Locate and identify every blood parasite.
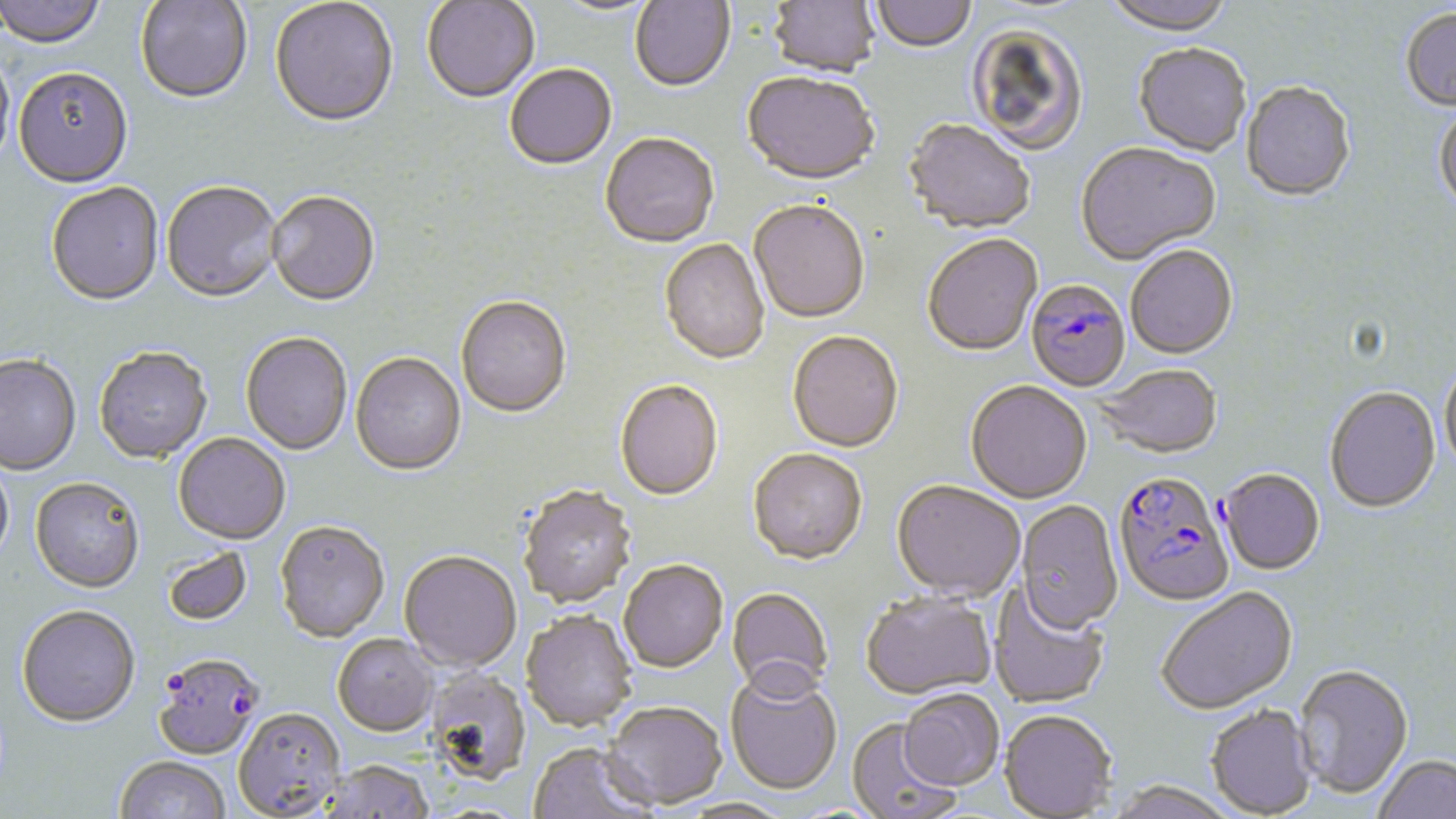

Approximate bounding boxes as (x1, y1, x2, y2) in pixels.
Plasmodium falciparum-infected red blood cells: (1026, 279, 1131, 393), (1218, 469, 1325, 576), (1113, 471, 1235, 609), (152, 653, 264, 762).
No Plasmodium ovale, Plasmodium malariae, Plasmodium vivax, Babesia divergens, or Trypanosoma brucei observed.

Uninfected red blood cell locations: (0, 0, 106, 51), (134, 0, 253, 107), (270, 0, 399, 130), (630, 0, 735, 93), (768, 0, 880, 80), (871, 0, 976, 55), (1102, 0, 1236, 39), (422, 1, 540, 105), (546, 1, 663, 18), (1400, 8, 1456, 114), (967, 24, 1090, 156), (1133, 46, 1251, 158), (0, 49, 14, 179), (505, 66, 617, 172), (13, 70, 133, 190), (741, 74, 879, 188), (1241, 82, 1355, 203), (1434, 104, 1456, 217), (904, 121, 1036, 235), (600, 135, 720, 250), (1076, 144, 1221, 267), (161, 183, 282, 305), (46, 184, 165, 308), (267, 193, 380, 308), (749, 202, 870, 325), (922, 236, 1043, 358), (659, 239, 770, 367), (1126, 246, 1238, 361), (455, 298, 572, 420), (787, 332, 903, 453), (240, 334, 352, 456), (93, 348, 212, 465), (350, 353, 466, 477), (0, 356, 82, 476), (1439, 360, 1456, 477), (1094, 365, 1224, 459), (615, 381, 723, 502), (965, 381, 1092, 504), (1325, 386, 1441, 513), (173, 433, 291, 545), (747, 449, 867, 565), (0, 453, 14, 572), (30, 479, 145, 595), (891, 480, 1025, 601), (518, 487, 638, 610), (1015, 500, 1123, 634), (275, 522, 390, 643), (161, 546, 253, 627), (399, 552, 521, 673), (619, 561, 727, 673), (989, 584, 1110, 709), (1157, 586, 1298, 716), (727, 587, 834, 699), (860, 592, 997, 701), (15, 606, 141, 728), (520, 611, 638, 733), (332, 635, 439, 738), (1294, 664, 1413, 799), (424, 669, 532, 786), (724, 671, 842, 796), (899, 691, 1005, 793), (600, 702, 727, 811), (1206, 704, 1316, 817), (233, 709, 346, 818), (999, 711, 1117, 818), (846, 719, 960, 819), (527, 744, 656, 819), (1372, 754, 1456, 819), (114, 757, 231, 819), (316, 761, 435, 819), (1103, 782, 1238, 819), (676, 799, 793, 819). Slide-level diagnosis: Plasmodium falciparum. Thin blood smear. May-Grünwald-Giemsa-stained preparation. 1000x magnification. Image is 1456×819 pixels. Optical microscopy. One field of a larger specimen.